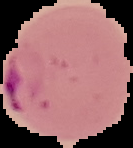
preparation = thin blood smear
image type = segmented cell region with the area outside set to black
image size = 133×148 pixels
result = Plasmodium parasites detected